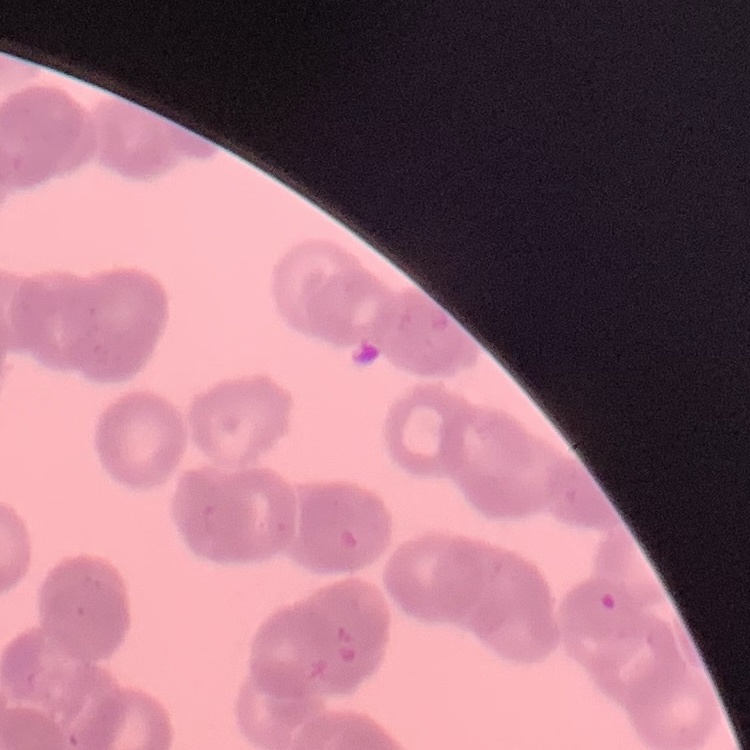
Summary:
  - Erythrocyte morphology: rouleaux formation
  - Stain: Field's or Giemsa
  - Image type: square crop of a larger photomicrograph
  - Preparation: thin blood smear